Mark where platelets are.
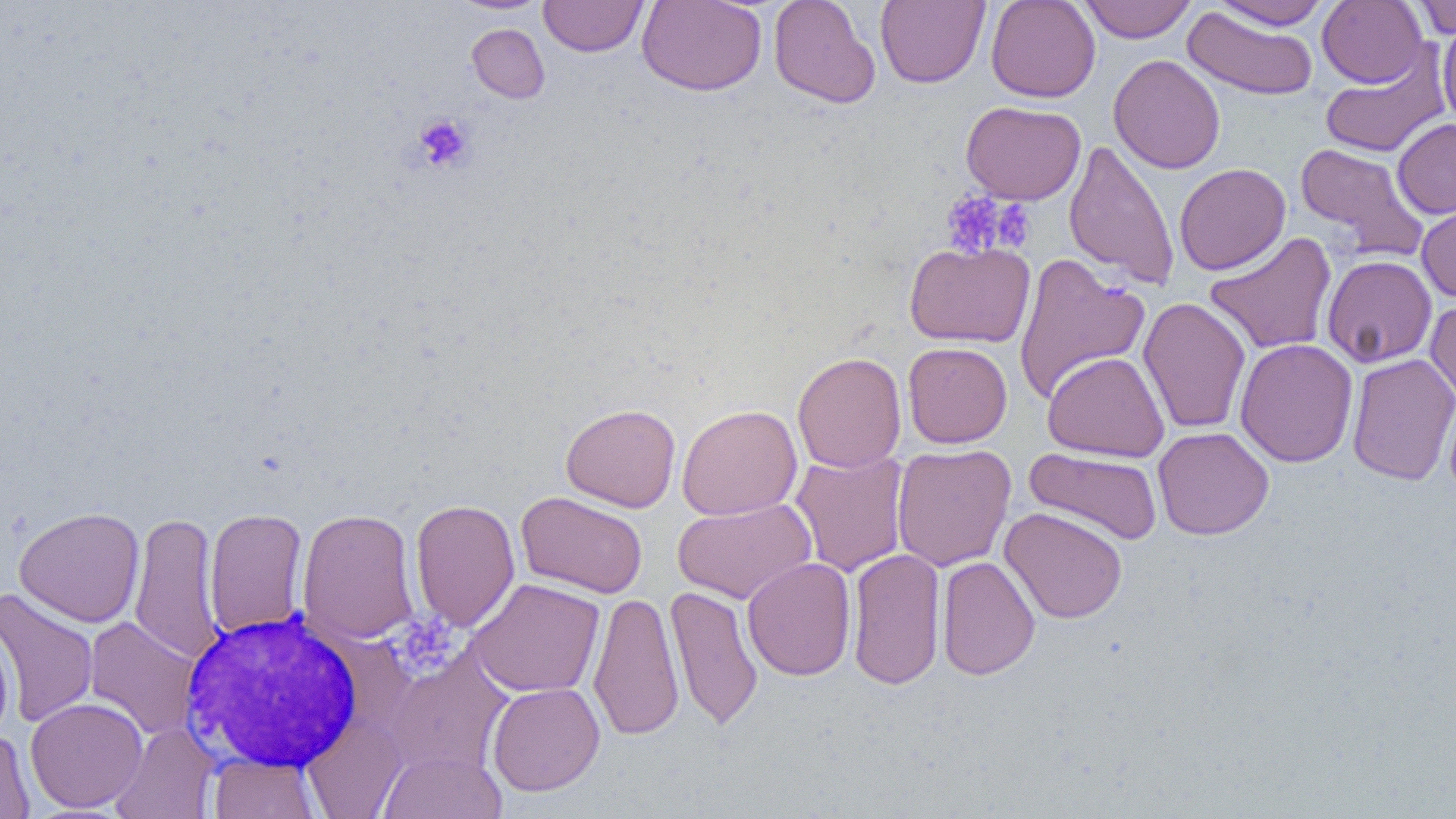
Approximate bounding boxes as [x1, y1, x2, y2] in pixels.
Platelets: [414, 112, 474, 172], [942, 191, 1014, 258], [992, 200, 1036, 252], [392, 613, 461, 674].

White blood cell locations: [176, 609, 371, 774]. Uninfected red blood cell locations: [444, 0, 557, 14], [538, 0, 649, 57], [636, 0, 767, 96], [768, 0, 880, 108], [875, 0, 990, 88], [985, 0, 1101, 103], [1079, 0, 1196, 43], [1211, 1, 1332, 30], [1317, 1, 1428, 88], [1412, 1, 1456, 39], [1183, 6, 1319, 101], [1438, 16, 1456, 132], [466, 23, 550, 103], [1320, 45, 1452, 159], [1108, 54, 1225, 174], [960, 101, 1086, 204], [1392, 119, 1456, 218], [1063, 139, 1180, 290], [1295, 142, 1430, 262], [1174, 163, 1291, 275], [1416, 198, 1456, 304], [1204, 231, 1337, 355], [904, 240, 1035, 348], [1012, 253, 1150, 404], [1321, 254, 1438, 368], [1137, 297, 1251, 434], [1425, 298, 1456, 406], [1234, 338, 1358, 468], [902, 342, 1012, 448], [1042, 351, 1170, 462], [792, 352, 907, 473], [1345, 353, 1456, 485], [1441, 385, 1456, 501], [561, 403, 681, 512], [677, 404, 802, 519], [1153, 427, 1274, 540], [891, 443, 1016, 572], [1024, 447, 1164, 546], [789, 450, 909, 577], [515, 491, 647, 599], [672, 498, 817, 604], [410, 499, 520, 632], [13, 506, 145, 627], [999, 506, 1128, 624], [297, 507, 420, 646], [204, 508, 309, 639], [129, 510, 224, 665], [846, 548, 946, 690], [936, 556, 1040, 680], [742, 557, 856, 681], [466, 578, 605, 698], [665, 585, 763, 731], [1, 588, 99, 729], [588, 590, 684, 740], [84, 616, 202, 740], [0, 624, 14, 742], [384, 651, 514, 776], [486, 682, 605, 796], [25, 697, 148, 813], [301, 714, 408, 818], [109, 723, 219, 819], [0, 729, 36, 818], [378, 749, 506, 819], [207, 752, 321, 818]. Slide-level diagnosis: no evidence of blood parasites. Image is 1456×819 pixels. Thin blood film. One field of a larger specimen. 1000x magnification. Optical microscopy.